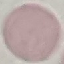

malaria status = uninfected
image type = cell patch, automatically extracted from a larger field of view and resized to 64 × 64 pixels
capture = smartphone through the microscope eyepiece
preparation = thin blood film
stain = Giemsa